Describe the morphology of the red blood cells.
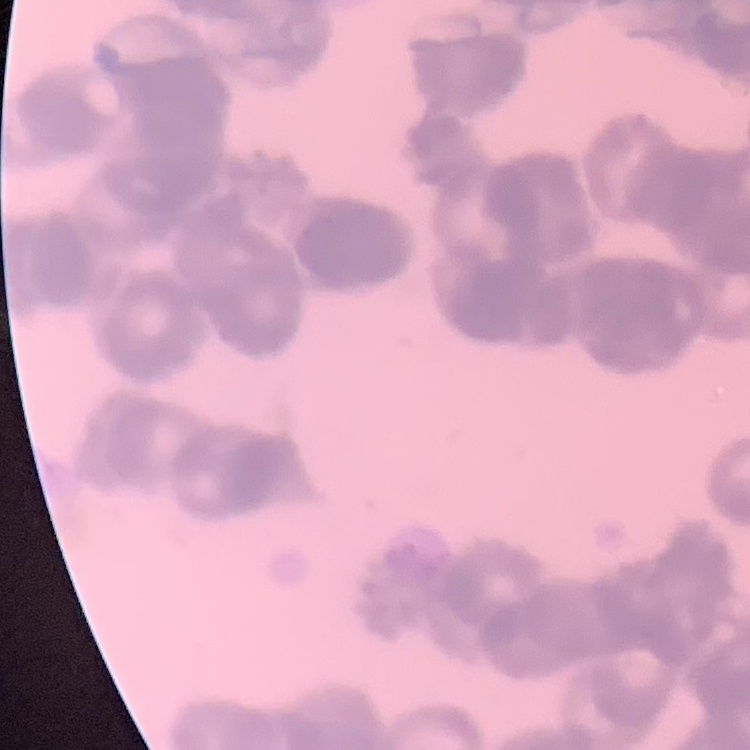

Rouleaux formation.

preparation = thin blood film
image type = square crop of a larger photomicrograph
stain = Field's or Giemsa